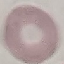
result = no malaria parasites detected
stain = Giemsa
preparation = thin smear
image type = automatically extracted cell patch, resized to 64 × 64 pixels
capture = smartphone through the microscope eyepiece